Describe the morphology of the red blood cells.
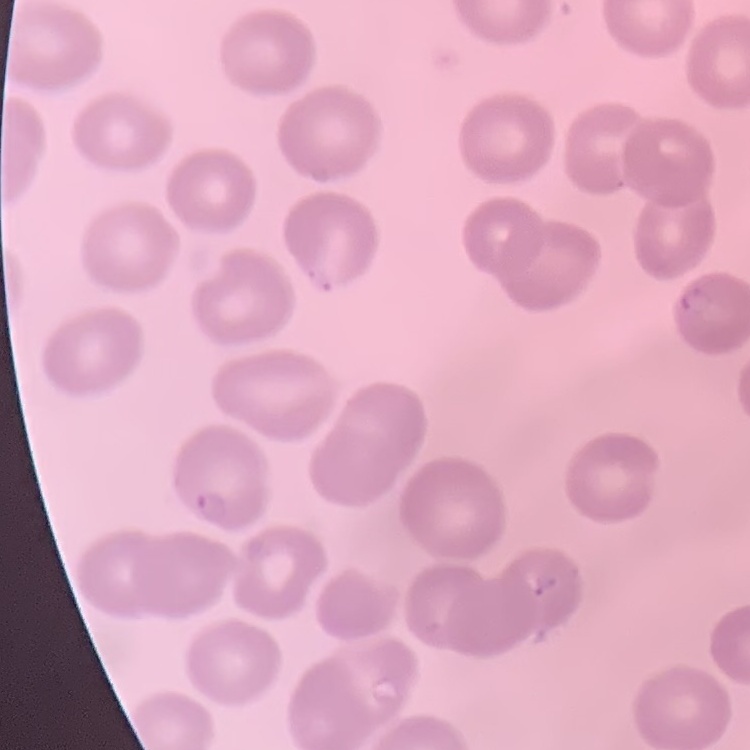
No rouleaux formation.

Thin peripheral smear. Field's or Giemsa stain. Square crop of a larger photomicrograph.